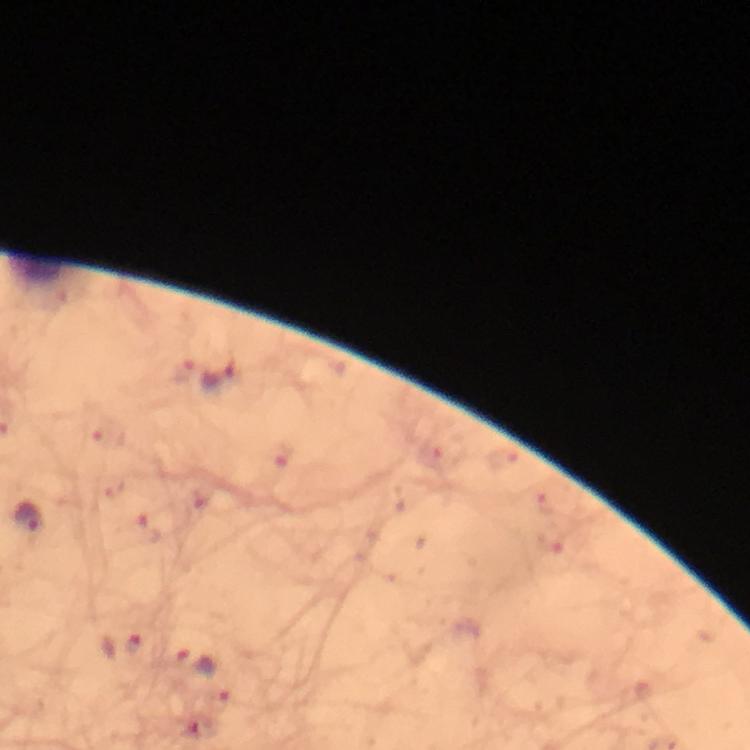 Approximate centers as (x, y) in pixels. Malaria parasite locations: (207, 372), (30, 521), (123, 645), (197, 662). From a diagnostic examination for malaria. Immersion oil applied. At 100x magnification. Giemsa-stained preparation. Cropped region of a single field of view. Image is 750×750 pixels. Smartphone photograph taken through a microscope. Thick blood film.